Locate every Plasmodium parasite.
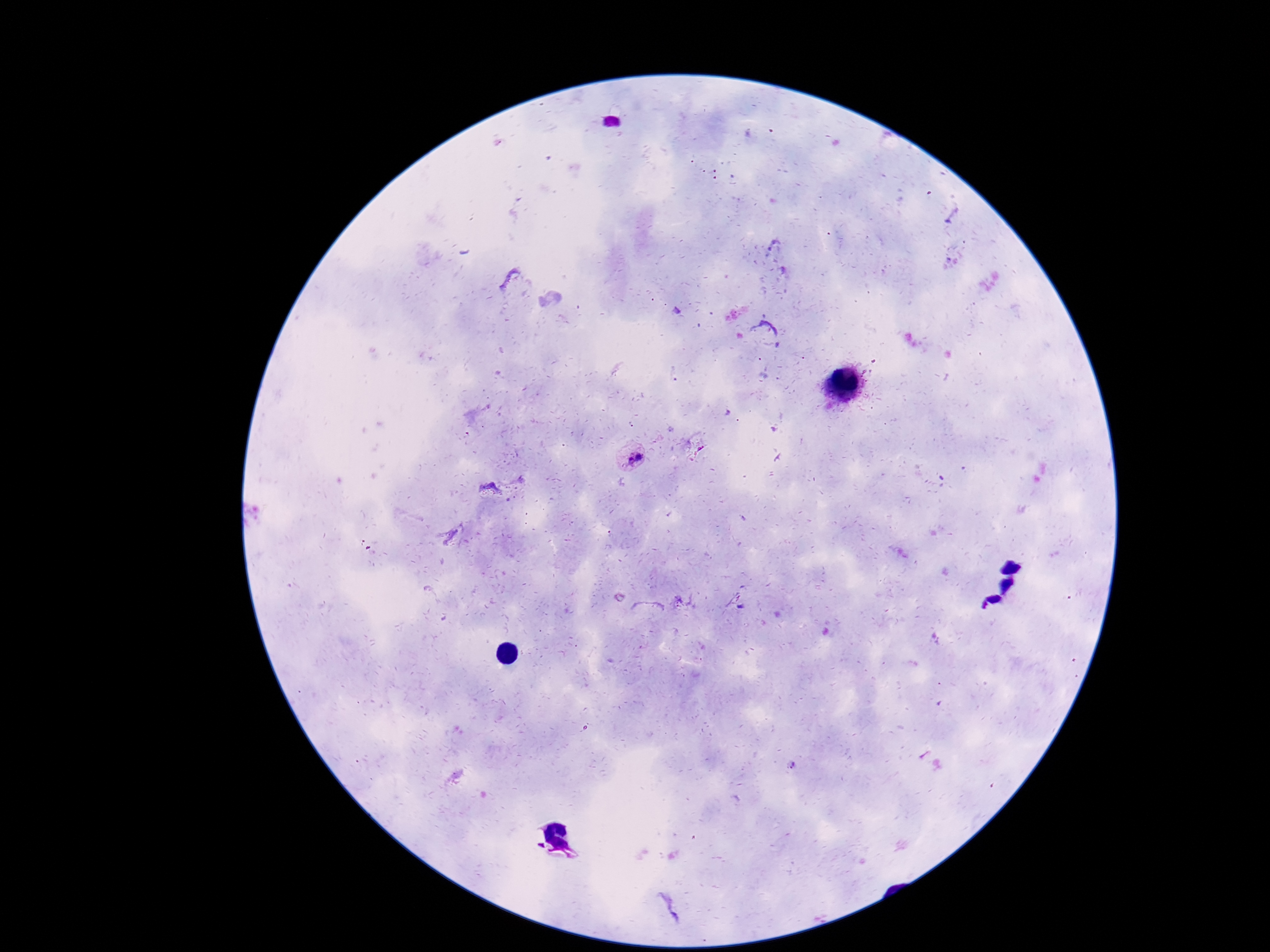

Approximate object centers, in pixels from the top-left corner.
Plasmodium parasites: (x=631, y=457).

Thick blood smear. Giemsa-stained preparation. Image is 1270×952 pixels. Patient malaria status: infected. Photographed through the microscope eyepiece with a smartphone camera. Single field of view. 100x magnification.